Give the location of every parasitized RBC.
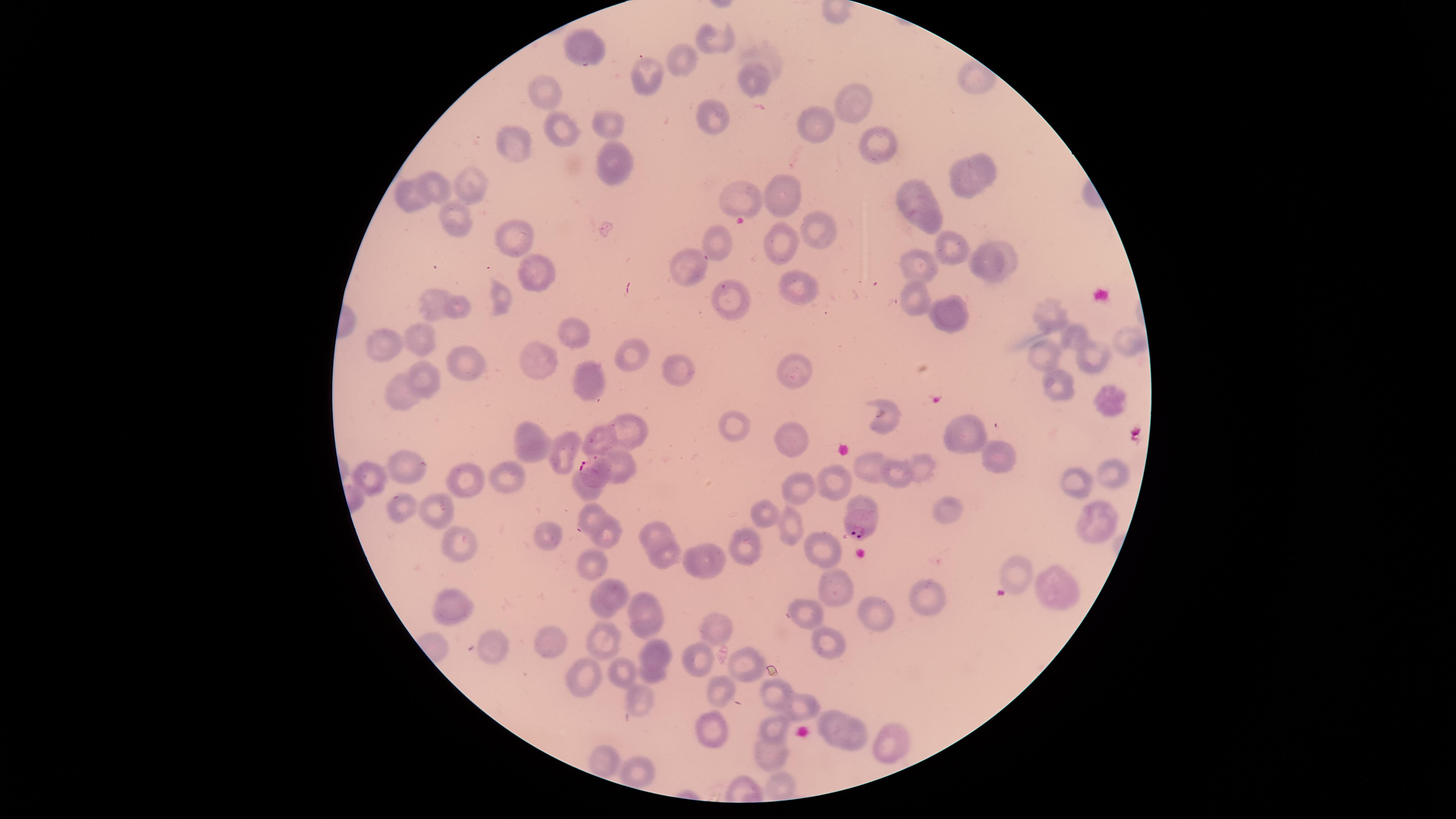

Approximate marker points, in pixels from the top-left corner.
Parasitized RBCs: (x=593, y=473), (x=862, y=522).

stain = Giemsa
field of view = single
image size = 1456×819 pixels
preparation = thin blood smear
uninfected RBCs = approximate marker points, in pixels from the top-left corner: (x=716, y=43), (x=590, y=52), (x=683, y=58), (x=643, y=78), (x=754, y=78), (x=544, y=91), (x=854, y=104), (x=607, y=122), (x=814, y=122), (x=711, y=123), (x=562, y=130), (x=876, y=140), (x=518, y=146), (x=610, y=165), (x=981, y=169), (x=440, y=184), (x=471, y=185), (x=959, y=186), (x=912, y=189), (x=739, y=192), (x=786, y=194), (x=398, y=196), (x=921, y=213), (x=459, y=220), (x=818, y=229), (x=516, y=235), (x=711, y=241), (x=786, y=243), (x=949, y=246), (x=1009, y=259), (x=981, y=262), (x=921, y=263), (x=688, y=268), (x=535, y=270), (x=798, y=285), (x=729, y=294), (x=916, y=297), (x=431, y=302), (x=502, y=302), (x=460, y=306), (x=948, y=309), (x=1054, y=313), (x=1072, y=331), (x=580, y=333), (x=1125, y=336), (x=422, y=337), (x=387, y=342), (x=1046, y=352), (x=630, y=353), (x=1093, y=356), (x=534, y=358), (x=463, y=361), (x=790, y=365), (x=675, y=368), (x=430, y=376), (x=588, y=378), (x=1058, y=383), (x=402, y=395), (x=1109, y=402), (x=888, y=408), (x=735, y=426), (x=629, y=427), (x=970, y=434), (x=601, y=439), (x=529, y=441), (x=796, y=444), (x=561, y=450), (x=993, y=453), (x=621, y=460), (x=923, y=465), (x=408, y=466), (x=873, y=466), (x=1109, y=469), (x=370, y=475), (x=507, y=477), (x=898, y=478), (x=798, y=480), (x=471, y=482), (x=1072, y=482), (x=835, y=484), (x=585, y=493), (x=438, y=510), (x=758, y=511), (x=403, y=512), (x=948, y=513), (x=587, y=516), (x=1095, y=524), (x=791, y=525), (x=605, y=531), (x=658, y=533), (x=546, y=534), (x=461, y=537), (x=747, y=543), (x=821, y=546), (x=665, y=552), (x=703, y=558), (x=592, y=567), (x=1018, y=572), (x=835, y=587), (x=1052, y=587), (x=616, y=595), (x=932, y=596), (x=643, y=603), (x=453, y=607), (x=599, y=610), (x=877, y=614), (x=812, y=615), (x=714, y=623), (x=650, y=625), (x=604, y=638), (x=553, y=640), (x=830, y=645), (x=492, y=647), (x=660, y=653), (x=694, y=655), (x=748, y=661), (x=620, y=670), (x=653, y=674), (x=583, y=678), (x=716, y=691), (x=778, y=694), (x=641, y=703), (x=806, y=704), (x=833, y=718), (x=775, y=725), (x=713, y=728), (x=856, y=733), (x=882, y=735), (x=774, y=750), (x=600, y=759), (x=643, y=767), (x=783, y=784)
capture = smartphone photograph through the microscope eyepiece
species = Plasmodium falciparum
visible region = circular